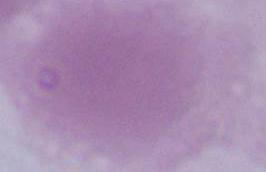

magnification = 1000x
identification = erythrocyte
modality = photomicrograph